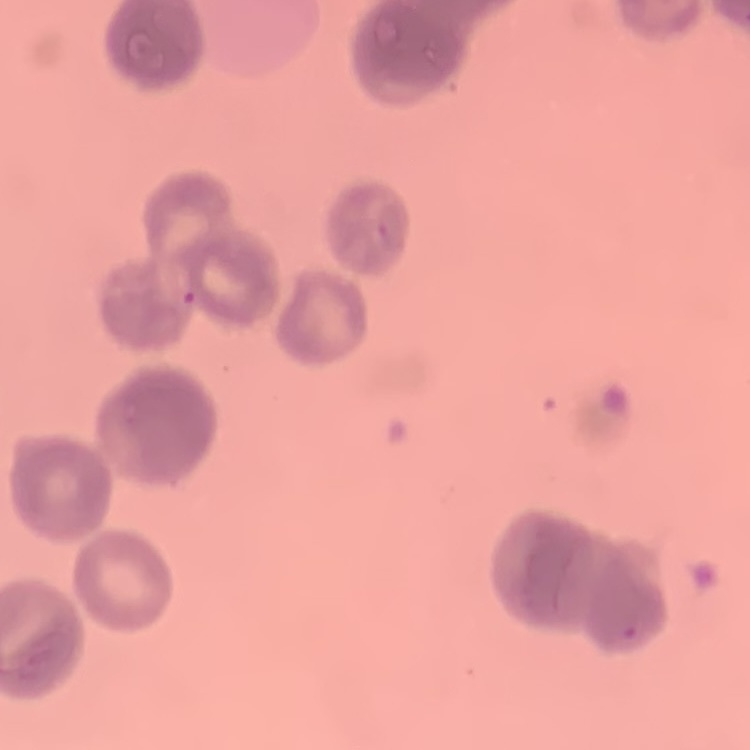

erythrocyte morphology = rouleaux formation
stain = Field's or Giemsa
preparation = thin blood smear
image type = one tile cut from a larger photomicrograph